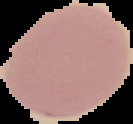

image size = 133×124 pixels
image type = segmented cell region with the area outside set to black
preparation = thin blood film
malaria status = uninfected